Locate every Plasmodium parasite.
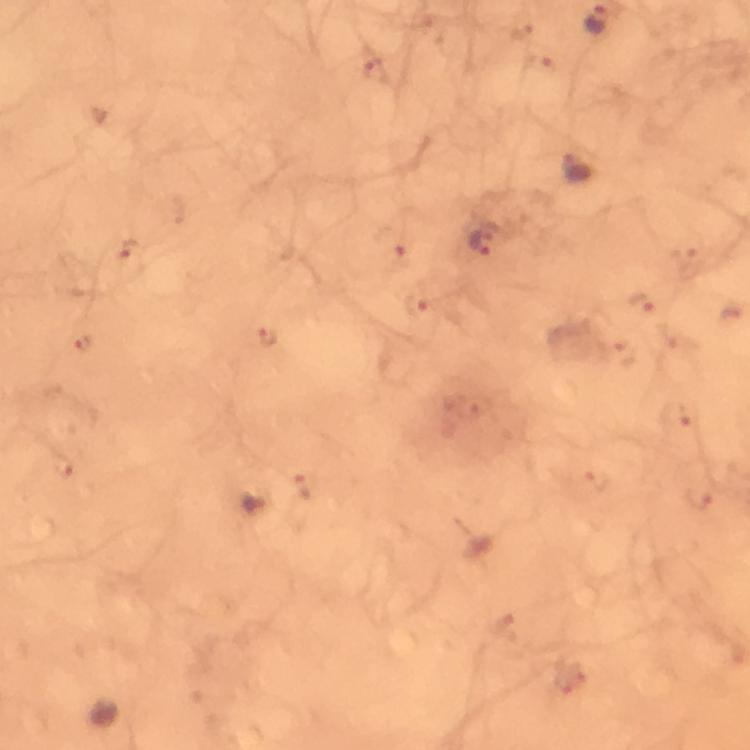
Approximate centers as {x, y} in pixels.
Plasmodium parasites: {577, 168}, {482, 241}.

capture: smartphone photograph through a microscope
immersion_oil: applied
image_size: 750×750 pixels
magnification: 100x
cropped_from: one field of view
stain: Giemsa
preparation: thick blood film
context: from a malaria diagnostic workup